Give the extent of all Plasmodium falciparum-infected red blood cells.
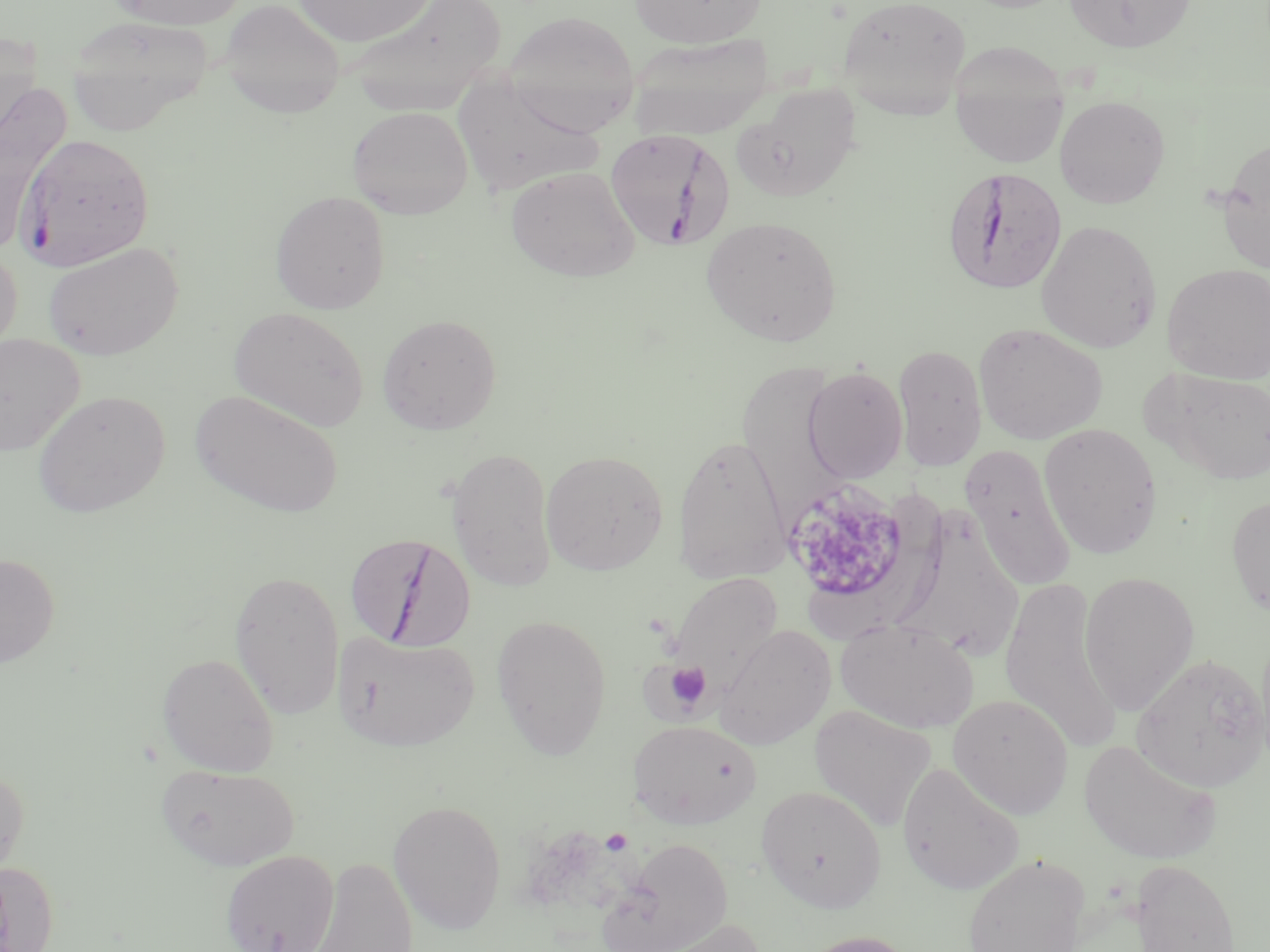

Approximate bounding boxes as (x1,y1)-(x2,y2) corner pairs in pixels.
Plasmodium falciparum-infected red blood cells: (603,129)-(733,250), (16,132)-(155,271), (942,166)-(1067,296), (345,533)-(477,653).

Uninfected red blood cell locations: (110,0)-(247,29), (219,0)-(345,118), (294,0)-(436,48), (341,0)-(505,114), (630,0)-(766,49), (837,0)-(971,116), (1064,0)-(1197,53), (503,10)-(639,133), (65,15)-(214,135), (627,32)-(775,141), (951,38)-(1068,167), (437,60)-(612,193), (0,82)-(72,251), (734,84)-(863,202), (1054,94)-(1171,208), (347,105)-(473,219), (1216,139)-(1270,273), (506,166)-(639,281), (270,190)-(391,314), (701,215)-(843,346), (1036,219)-(1163,353), (43,241)-(184,361), (0,248)-(22,360), (1162,262)-(1270,384), (229,306)-(370,432), (377,313)-(501,435), (973,322)-(1108,444), (0,334)-(85,455), (893,343)-(987,471), (742,353)-(850,528), (802,366)-(908,484), (1146,366)-(1270,485), (32,389)-(170,519), (190,389)-(345,519), (1038,422)-(1163,558), (672,432)-(791,584), (961,443)-(1078,591), (446,447)-(557,591), (540,450)-(669,575), (798,491)-(954,636), (1226,493)-(1270,620), (900,518)-(1024,659), (0,553)-(60,669), (229,569)-(345,719), (1079,570)-(1200,715), (666,571)-(784,698), (998,576)-(1122,752), (491,613)-(612,759), (835,619)-(979,732), (714,625)-(836,750), (332,631)-(480,751), (157,652)-(279,776), (1132,653)-(1269,791), (947,693)-(1074,819), (809,704)-(937,831), (627,719)-(762,829), (1078,738)-(1222,864), (0,761)-(30,886), (896,761)-(1025,895), (157,762)-(300,872), (756,784)-(886,911), (387,798)-(507,933), (600,838)-(734,952), (220,849)-(340,952), (962,853)-(1092,952), (307,856)-(419,951), (1129,858)-(1241,952), (0,860)-(60,952), (641,917)-(769,952), (796,930)-(919,952). Platelet locations: (780,478)-(915,613), (656,660)-(714,715), (600,828)-(633,855). Slide-level diagnosis: Plasmodium falciparum. Image is 1270×952 pixels. Single field of view. Thin blood smear. May-Grünwald-Giemsa stain. 1000x magnification. Optical microscopy.